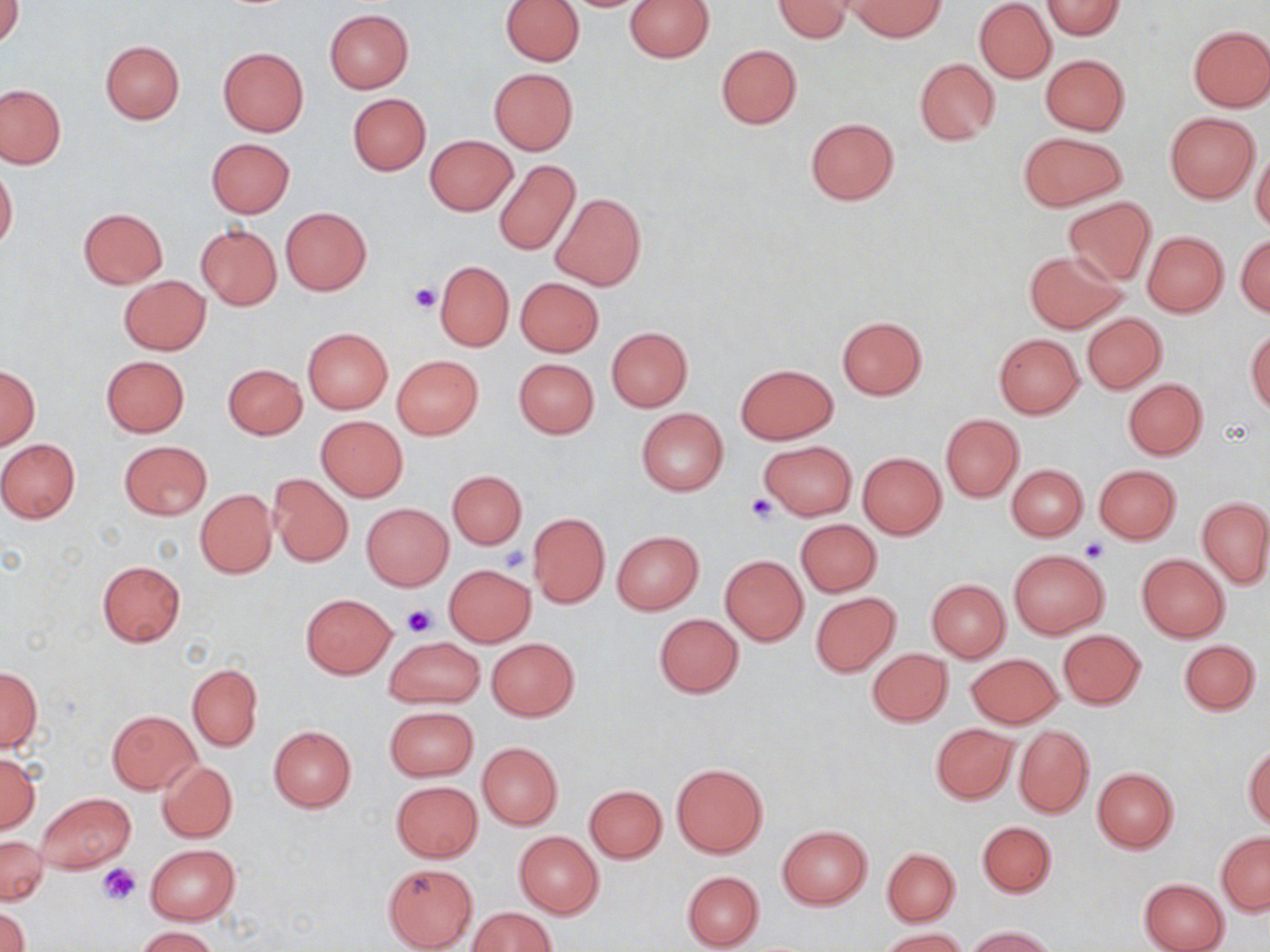
slide-level diagnosis = no evidence of blood parasites
preparation = thin blood smear
platelet locations = approximate bounding boxes as (x1, y1, x2, y2) in pixels: (408, 282, 441, 313), (745, 492, 781, 524), (1081, 539, 1107, 562), (499, 545, 531, 574), (402, 605, 436, 637), (99, 864, 141, 905)
image size = 1270×952 pixels
modality = light microscopy
magnification = 1000x
stain = May-Grünwald-Giemsa
field of view = one of a larger specimen
uninfected red blood cell locations = approximate bounding boxes as (x1, y1, x2, y2) in pixels: (1, 0, 24, 47), (500, 0, 584, 66), (624, 0, 714, 62), (773, 0, 853, 42), (845, 0, 946, 41), (974, 1, 1057, 84), (1040, 1, 1125, 39), (324, 9, 413, 94), (1187, 25, 1270, 111), (100, 39, 185, 124), (716, 44, 801, 129), (218, 47, 308, 136), (1041, 54, 1129, 135), (914, 57, 999, 145), (489, 68, 577, 154), (0, 84, 65, 168), (347, 92, 431, 175), (1165, 113, 1259, 202), (804, 118, 900, 204), (1018, 132, 1126, 211), (426, 135, 517, 217), (207, 138, 294, 217), (1251, 148, 1270, 234), (494, 160, 580, 257), (0, 165, 18, 251), (551, 193, 646, 291), (1063, 197, 1156, 285), (77, 207, 169, 288), (281, 208, 371, 295), (196, 223, 282, 310), (1142, 230, 1229, 317), (1236, 235, 1270, 317), (1023, 250, 1128, 333), (434, 261, 515, 351), (119, 275, 210, 355), (515, 277, 603, 356), (1081, 313, 1166, 393), (836, 315, 927, 399), (606, 326, 692, 411), (302, 327, 394, 413), (1246, 329, 1270, 415), (993, 333, 1084, 419), (101, 355, 189, 437), (393, 356, 483, 438), (513, 358, 599, 438), (734, 363, 837, 444), (223, 364, 307, 440), (0, 367, 40, 448), (1122, 378, 1207, 460), (636, 408, 728, 495), (941, 415, 1023, 502), (315, 416, 408, 501), (0, 438, 80, 523), (759, 439, 855, 519), (118, 440, 212, 519), (858, 452, 947, 539), (1007, 464, 1087, 541), (1093, 464, 1182, 544), (448, 470, 527, 548), (268, 473, 353, 567), (195, 488, 277, 578), (1198, 497, 1270, 589), (361, 503, 454, 590), (527, 513, 610, 608), (796, 518, 882, 596), (612, 531, 704, 614), (1009, 549, 1108, 638), (1137, 554, 1229, 642), (721, 556, 808, 644), (97, 560, 185, 646), (445, 564, 535, 646), (927, 579, 1010, 661), (810, 592, 901, 678), (302, 594, 397, 678), (654, 614, 743, 698), (1058, 629, 1146, 710), (385, 636, 485, 708), (486, 637, 579, 721), (1179, 639, 1261, 715), (866, 648, 953, 727), (967, 653, 1063, 728), (187, 663, 263, 751), (0, 666, 42, 753), (385, 706, 478, 781), (107, 710, 200, 794), (930, 723, 1018, 803), (268, 725, 357, 811), (1013, 725, 1094, 818), (477, 742, 563, 829), (1243, 743, 1270, 828), (0, 753, 40, 834), (157, 759, 237, 843), (671, 763, 768, 859), (1091, 767, 1179, 854), (391, 781, 483, 862), (584, 785, 667, 863), (36, 792, 135, 874), (977, 820, 1056, 898), (777, 825, 871, 909), (514, 831, 603, 917), (1217, 832, 1269, 915), (0, 836, 47, 905), (145, 844, 239, 924), (882, 846, 960, 925), (382, 862, 478, 950), (681, 871, 762, 949), (1139, 877, 1229, 952), (1, 906, 31, 952), (469, 907, 558, 951), (134, 926, 220, 952), (967, 926, 1058, 951), (880, 928, 967, 952)